State which parasite is depicted.
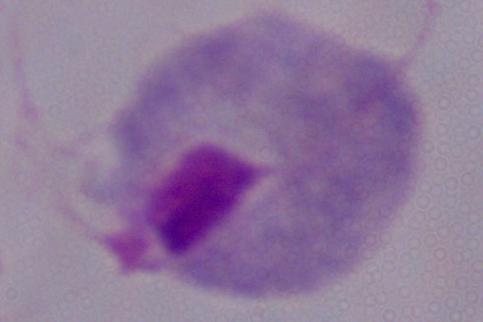

This is a trichomonad.

Summary:
  - Magnification: 1000x
  - Modality: photomicrograph